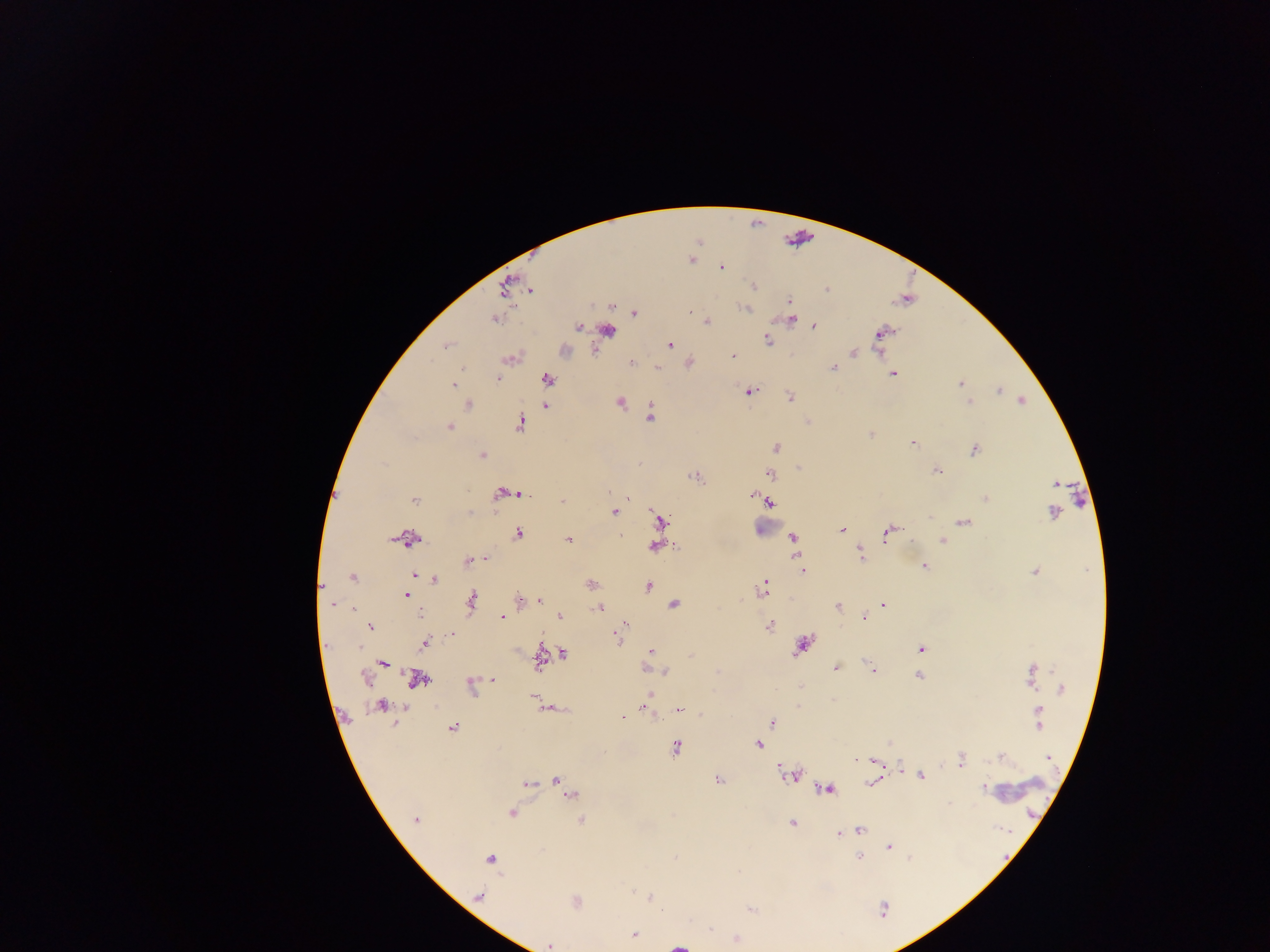
country = Ghana
malaria parasite locations = approximate centers as {x, y} in pixels: {692, 260}, {721, 268}, {754, 285}, {827, 289}, {530, 290}, {789, 301}, {745, 308}, {690, 312}, {634, 313}, {493, 319}, {791, 319}, {706, 321}, {578, 326}, {814, 326}, {882, 333}, {767, 340}, {669, 345}, {445, 346}, {878, 348}, {853, 352}, {732, 356}, {509, 359}, {631, 363}, {657, 367}, {833, 367}, {893, 374}, {497, 379}, {548, 379}, {961, 383}, {453, 385}, {999, 391}, {750, 392}, {790, 396}, {1022, 400}, {620, 402}, {968, 402}, {468, 405}, {545, 406}, {651, 416}, {520, 424}, {449, 428}, {871, 434}, {913, 444}, {775, 447}, {974, 450}, {482, 455}, {798, 468}, {936, 471}, {771, 474}, {695, 477}, {610, 492}, {502, 494}, {523, 495}, {753, 495}, {985, 498}, {414, 500}, {562, 500}, {769, 502}, {614, 512}, {1053, 512}, {929, 516}, {660, 521}, {965, 522}, {842, 529}, {887, 533}, {518, 534}, {622, 537}, {792, 537}, {408, 539}, {568, 540}, {942, 541}, {655, 546}, {860, 554}, {486, 560}, {469, 561}, {924, 566}, {803, 570}, {1034, 572}, {415, 575}, {353, 577}, {435, 579}, {591, 585}, {647, 586}, {762, 589}, {406, 595}, {520, 601}, {538, 601}, {472, 602}, {332, 604}, {674, 604}, {884, 605}, {837, 606}, {353, 608}, {599, 608}, {419, 615}, {559, 616}, {501, 617}, {865, 618}, {625, 624}, {769, 626}, {370, 627}, {451, 635}, {618, 637}, {424, 643}, {801, 647}, {360, 648}, {920, 649}, {650, 651}, {563, 654}, {539, 660}, {383, 663}, {869, 666}, {836, 668}, {872, 671}, {665, 672}, {919, 676}, {1032, 676}, {366, 677}, {492, 679}, {417, 680}, {471, 687}, {1062, 689}, {650, 694}, {533, 697}, {381, 706}, {645, 706}, {678, 709}, {622, 717}, {1039, 718}, {772, 722}, {452, 729}, {758, 744}, {676, 748}, {1001, 756}, {1049, 758}, {961, 759}, {874, 762}, {900, 766}, {791, 775}, {921, 776}, {556, 779}, {717, 780}, {871, 782}, {527, 784}, {983, 788}, {827, 789}, {571, 795}, {511, 813}, {414, 820}, {582, 820}, {791, 823}, {860, 830}, {850, 831}, {839, 833}, {889, 847}, {859, 858}, {490, 859}, {632, 892}, {479, 895}, {650, 897}, {576, 901}, {751, 909}, {883, 909}, {634, 935}, {737, 939}, {549, 945}
field of view = single
preparation = thick blood film
leukocyte locations = approximate centers as {x, y} in pixels: {608, 335}, {766, 525}, {1017, 789}
capture = mobile-phone photograph through a microscope
object labeled both malaria parasite and leukocyte by the source = approximate centers as {x, y} in pixels: {679, 945}
image size = 1270×952 pixels